Locate leukocytes (white blood cells).
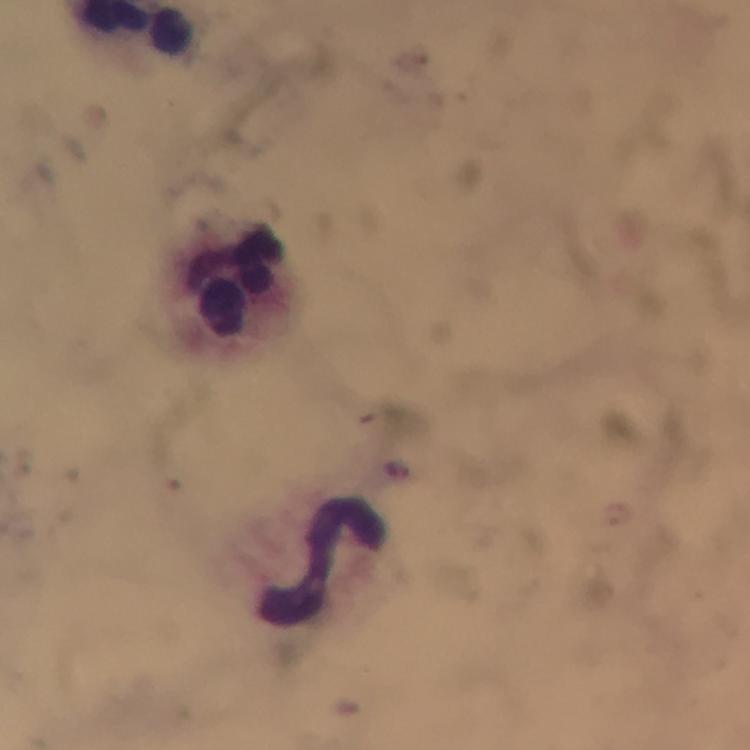
Approximate centers as (x, y) in pixels.
Leukocytes: (232, 277), (323, 566).

cropped from = a single field of view
capture = smartphone photograph through a microscope
Plasmodium parasite locations = approximate centers as (x, y) in pixels: (398, 468)
magnification = 100x
preparation = thick blood film
immersion oil = applied
context = from a malaria diagnostic workup
stain = Giemsa
image size = 750×750 pixels